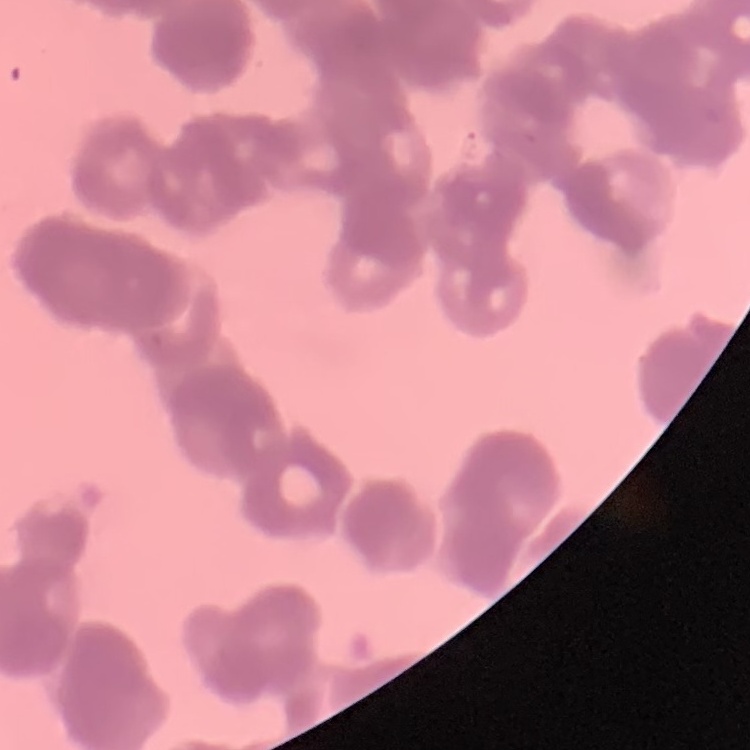

erythrocyte morphology = rouleaux formation
preparation = thin peripheral smear
stain = Field's or Giemsa
image type = square crop of a larger photomicrograph